Assess for Plasmodium parasites.
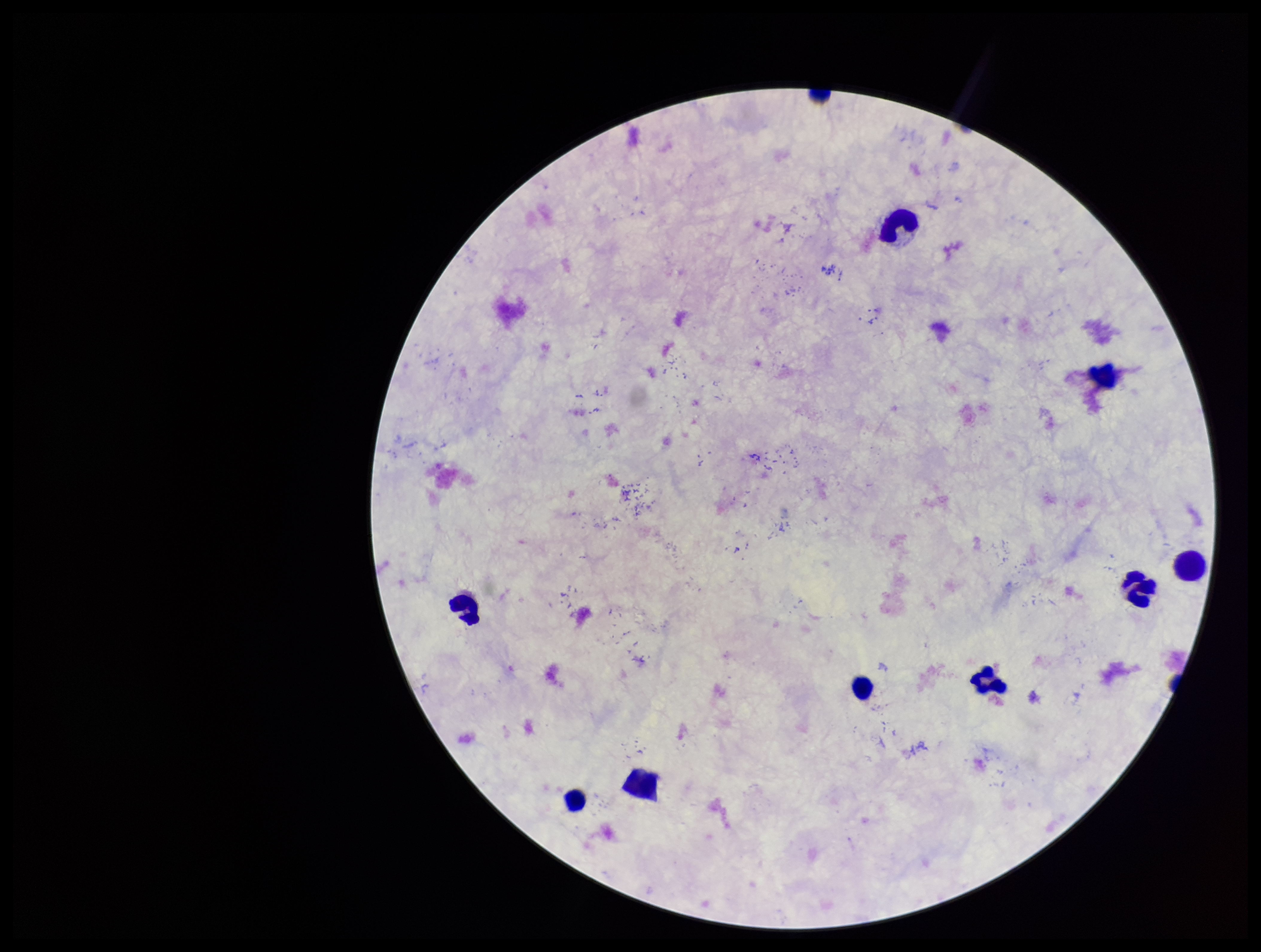
None seen.

Summary:
  - Leukocyte count: 9
  - Capture: smartphone photograph through the microscope eyepiece
  - Image size: 1261×952 pixels
  - Preparation: thick
  - Field of view: one from this slide
  - Patient malaria status: negative
  - Parasite count: 0
  - Stain: Giemsa